Classify this cell by malaria status.
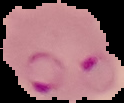

It is parasitized.

Summary:
  - Image size: 124×103 pixels
  - Preparation: thin blood film
  - Image type: cell region segmented out of the field of view; surrounding area masked to black